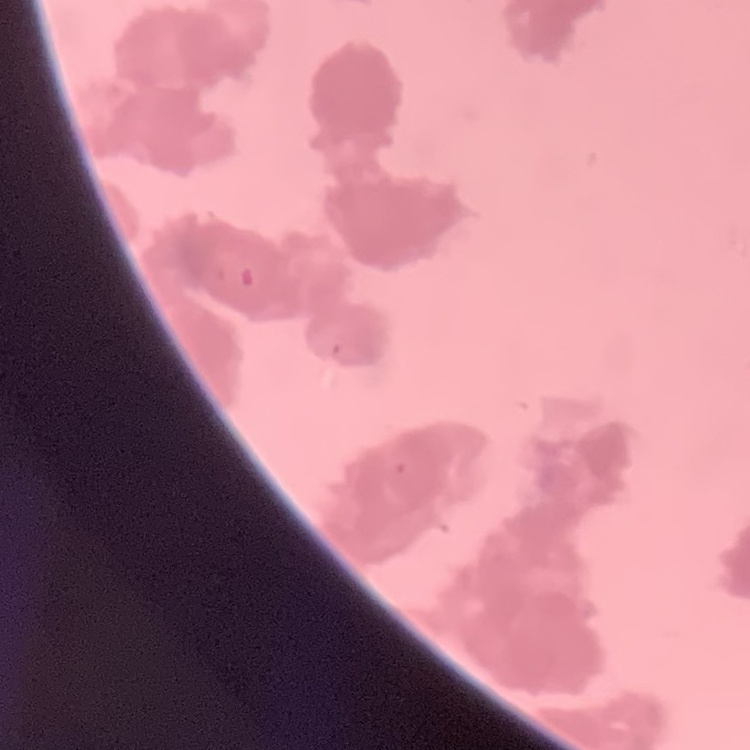
The red blood cells exhibit rouleaux formation. Square crop of a larger photomicrograph. Thin blood film. Field's or Giemsa stain.